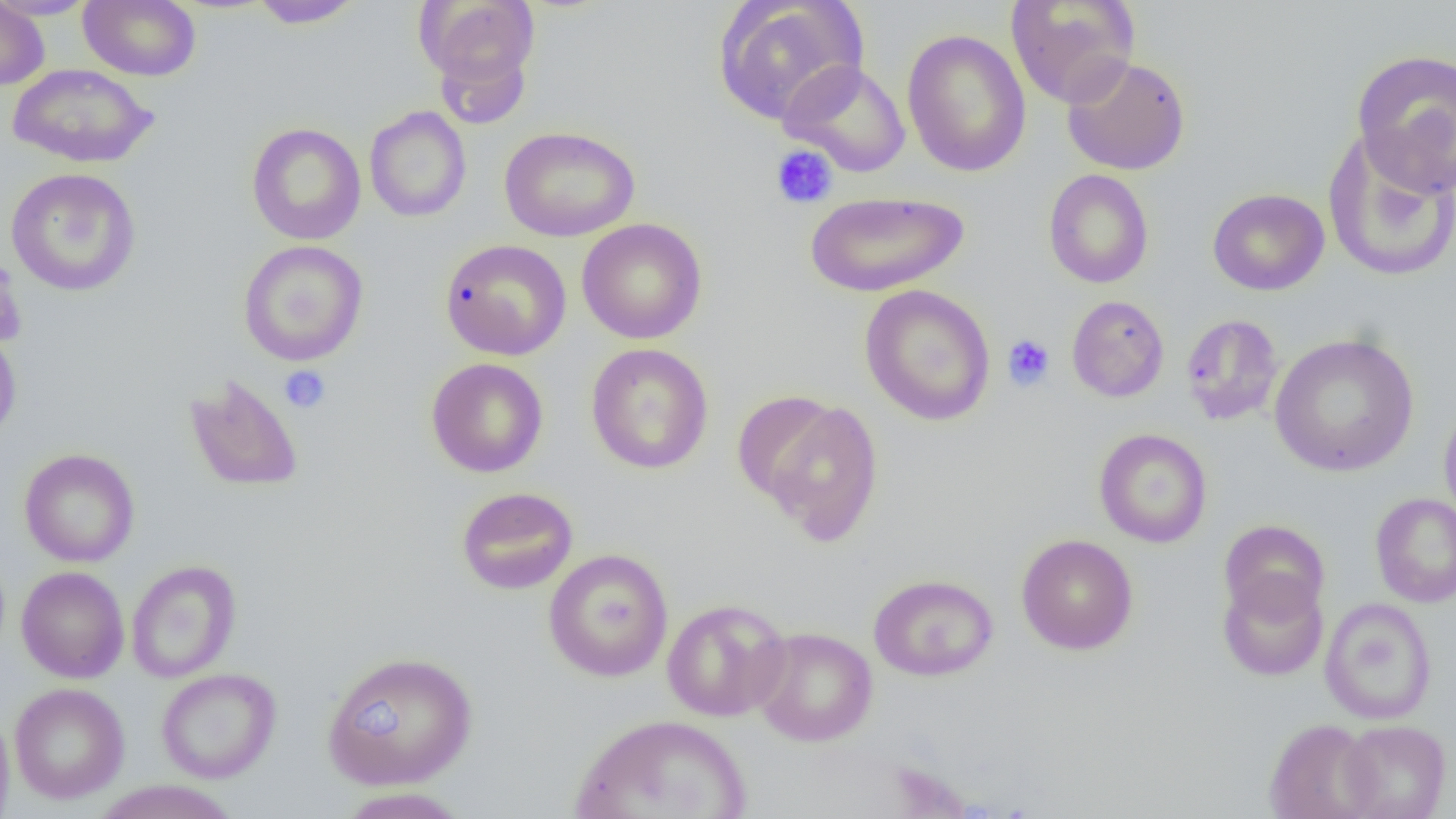
Approximate bounding boxes as (x1, y1, x2, y2) in pixels. Platelet locations: (770, 144, 838, 209), (1002, 334, 1055, 391), (279, 365, 331, 415). Uninfected red blood cell locations: (0, 0, 100, 20), (79, 0, 201, 81), (416, 0, 540, 97), (713, 0, 869, 126), (1005, 0, 1140, 109), (0, 1, 50, 90), (250, 1, 365, 29), (902, 28, 1031, 178), (1351, 49, 1456, 196), (1062, 54, 1190, 175), (780, 59, 911, 177), (8, 64, 158, 167), (364, 106, 472, 222), (246, 123, 366, 245), (499, 125, 639, 241), (1323, 128, 1456, 282), (6, 167, 141, 296), (1043, 169, 1154, 288), (1207, 188, 1330, 295), (804, 191, 969, 297), (576, 218, 708, 345), (440, 238, 572, 361), (238, 240, 369, 366), (0, 250, 28, 350), (859, 284, 996, 427), (1066, 294, 1169, 402), (1180, 313, 1285, 426), (0, 321, 22, 443), (1269, 332, 1419, 477), (586, 343, 714, 474), (426, 358, 549, 478), (184, 373, 304, 493), (742, 393, 885, 545), (1439, 400, 1456, 526), (1094, 428, 1212, 548), (19, 448, 140, 567), (455, 486, 579, 595), (1370, 493, 1456, 607), (1219, 519, 1330, 622), (1015, 534, 1139, 655), (543, 549, 674, 682), (126, 559, 241, 683), (16, 566, 129, 683), (1217, 572, 1328, 682), (868, 573, 998, 681), (1319, 597, 1437, 725), (662, 598, 791, 721), (751, 626, 878, 746), (321, 650, 479, 789), (156, 667, 281, 783), (9, 682, 129, 804), (0, 708, 15, 818), (569, 713, 752, 819), (1264, 718, 1380, 819), (1337, 719, 1451, 818), (91, 780, 242, 819), (334, 787, 472, 818). Slide-level diagnosis: negative for blood parasites. Thin blood film. Image is 1456×819 pixels. Single field of view. 1000x magnification. Light microscopy.